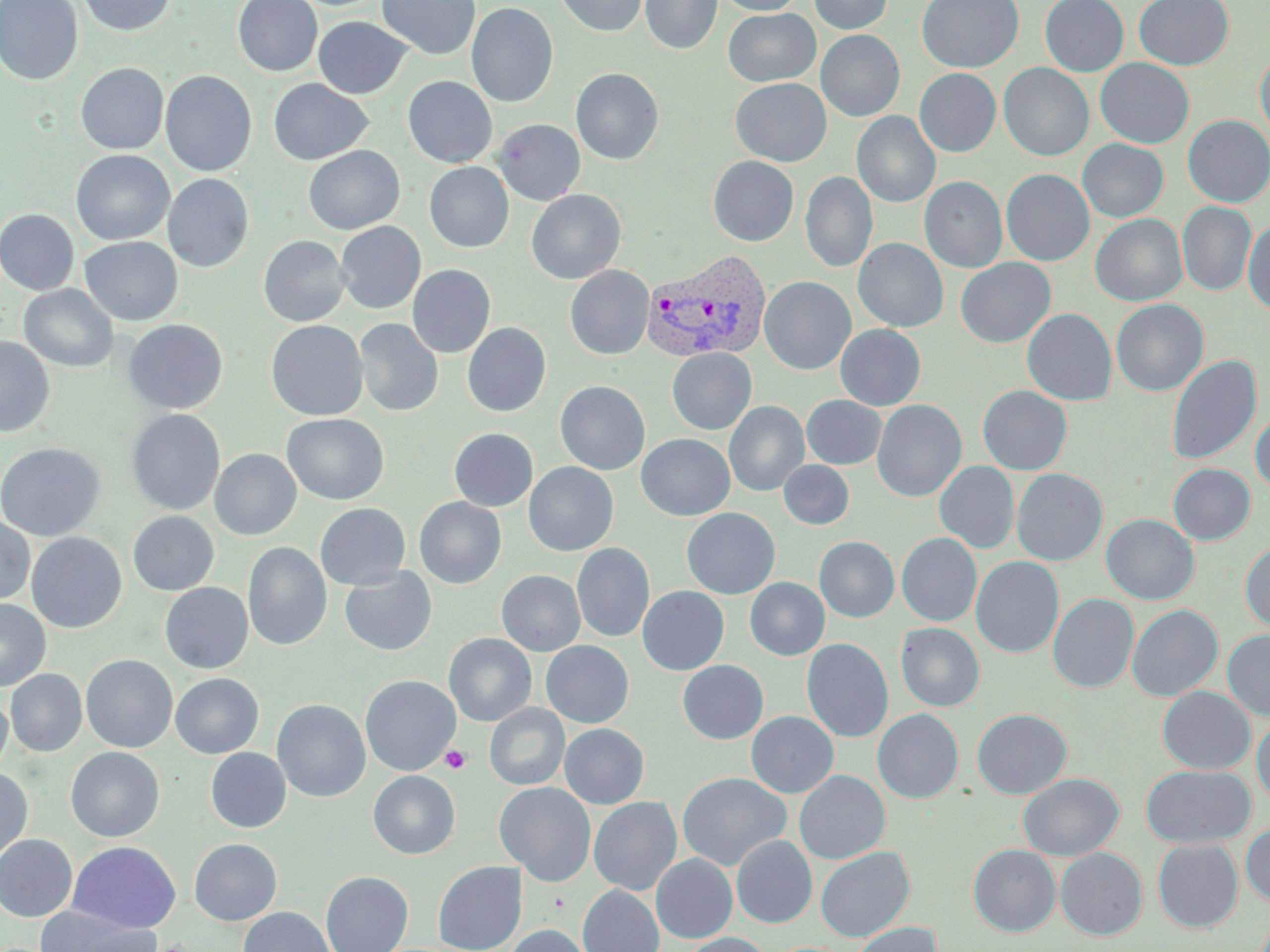
Summary:
  - Coordinate format: approximate bounding boxes as (x1,y1)-(x2,y2) corner pairs in pixels
  - Platelet locations: (440,746)-(471,774)
  - Plasmodium vivax-infected red blood cell locations: (641,249)-(772,364)
  - Uninfected red blood cell locations: (0,0)-(83,85), (78,0)-(177,36), (233,0)-(322,76), (377,0)-(480,60), (555,0)-(648,36), (640,0)-(722,55), (715,0)-(805,15), (809,0)-(894,34), (917,0)-(1024,72), (1040,0)-(1128,76), (1134,0)-(1234,70), (466,3)-(558,108), (724,8)-(820,86), (313,16)-(412,98), (816,30)-(905,121), (1255,47)-(1270,142), (1095,58)-(1195,147), (76,63)-(168,154), (999,63)-(1094,161), (571,68)-(663,164), (915,68)-(1001,156), (161,70)-(257,177), (403,76)-(497,167), (269,78)-(373,165), (730,78)-(832,166), (852,112)-(940,207), (1183,115)-(1270,207), (493,119)-(585,206), (1077,139)-(1169,222), (303,146)-(405,235), (71,150)-(174,245), (708,156)-(799,246), (424,162)-(513,252), (1001,169)-(1094,266), (800,172)-(877,272), (162,173)-(253,272), (919,176)-(1007,273), (526,189)-(626,284), (1177,202)-(1256,296), (0,209)-(79,295), (1090,214)-(1187,306), (335,221)-(426,313), (1243,221)-(1270,316), (258,235)-(350,326), (80,236)-(183,325), (853,238)-(948,332), (956,257)-(1056,347), (408,265)-(495,358), (565,266)-(653,360), (759,276)-(856,374), (19,284)-(118,372), (1111,299)-(1208,396), (1022,309)-(1117,405), (354,318)-(443,417), (123,319)-(227,414), (266,320)-(368,420), (462,323)-(551,416), (836,325)-(925,410), (0,337)-(54,437), (667,348)-(756,434), (1167,355)-(1261,466), (555,381)-(650,475), (978,385)-(1072,475), (802,395)-(886,469), (872,399)-(966,501), (724,401)-(809,496), (127,409)-(225,515), (1251,410)-(1270,493), (282,413)-(389,504), (449,428)-(538,511), (636,434)-(735,520), (0,443)-(105,541), (210,449)-(301,540), (778,460)-(854,530), (935,461)-(1019,553), (523,462)-(618,556), (1168,463)-(1255,545), (1012,468)-(1107,565), (415,498)-(506,588), (315,503)-(410,590), (681,507)-(780,599), (128,511)-(219,596), (1101,513)-(1199,605), (0,515)-(35,605), (26,532)-(127,632), (897,533)-(982,626), (814,536)-(899,622), (1240,539)-(1270,634), (243,542)-(331,651), (572,543)-(654,641), (971,556)-(1064,657), (339,566)-(437,656), (496,570)-(585,656), (745,578)-(829,660), (160,583)-(253,673), (638,586)-(729,675), (1048,593)-(1138,693), (0,599)-(50,691), (1126,604)-(1223,702), (896,623)-(985,711), (1222,630)-(1270,720), (443,633)-(536,726), (802,638)-(893,743), (541,641)-(634,727), (81,654)-(178,752), (678,660)-(768,744), (6,669)-(87,756), (171,673)-(263,758), (360,675)-(461,775), (1157,687)-(1255,774), (0,689)-(11,775), (272,699)-(371,802), (485,703)-(570,790), (971,708)-(1072,799), (872,709)-(963,803), (746,711)-(838,797), (1252,712)-(1270,806), (559,723)-(649,808), (66,747)-(165,842), (206,747)-(290,833), (1142,765)-(1255,848), (0,767)-(32,865), (368,770)-(460,859), (794,770)-(890,863), (677,772)-(791,871), (1018,773)-(1123,861), (494,782)-(596,886), (589,797)-(682,895), (1241,823)-(1270,907), (0,834)-(77,921), (732,835)-(817,928), (189,839)-(282,925), (1153,839)-(1242,933), (68,841)-(181,933), (968,844)-(1060,937), (816,847)-(915,941), (1055,848)-(1147,940), (652,853)-(737,943), (433,861)-(527,952), (321,871)-(413,952), (578,885)-(664,952), (35,904)-(160,952), (238,906)-(335,952), (848,922)-(942,952), (502,925)-(593,952), (682,933)-(773,952)
  - Slide-level diagnosis: Plasmodium vivax
  - Field of view: single
  - Image size: 1270×952 pixels
  - Stain: May-Grünwald-Giemsa
  - Preparation: thin blood smear
  - Magnification: 1000x
  - Modality: light microscopy